State which cell type is depicted.
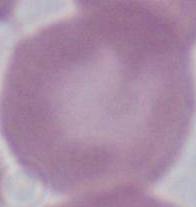

An erythrocyte.

Summary:
  - Modality: photomicrograph
  - Magnification: 1000x